State which parasite is depicted.
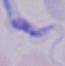

A trypanosome.

Summary:
  - Magnification: 1000x
  - Modality: micrograph